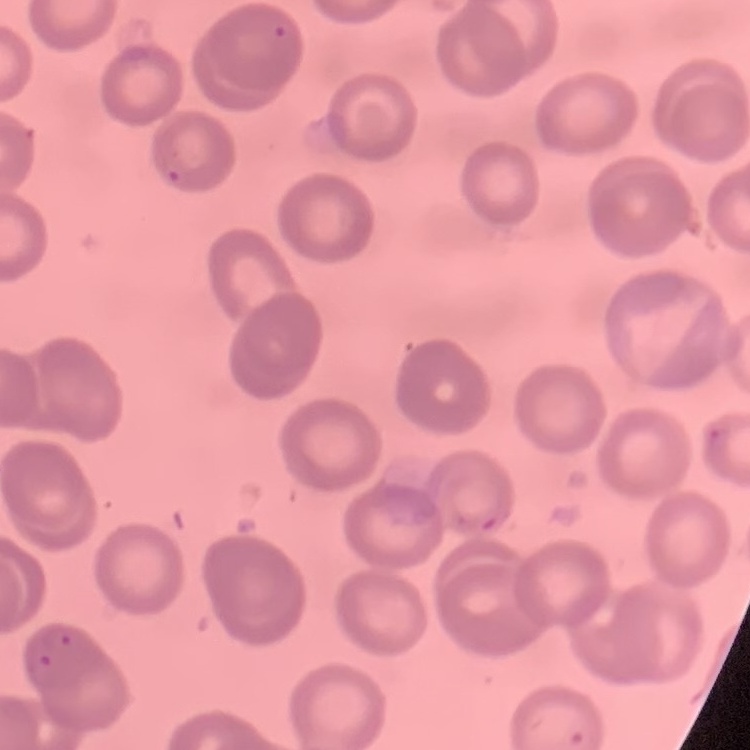

The erythrocytes show no rouleaux formation. Thin blood film. Stained with either Field's or Giemsa. Square crop of a larger photomicrograph.